Give the preparation type.
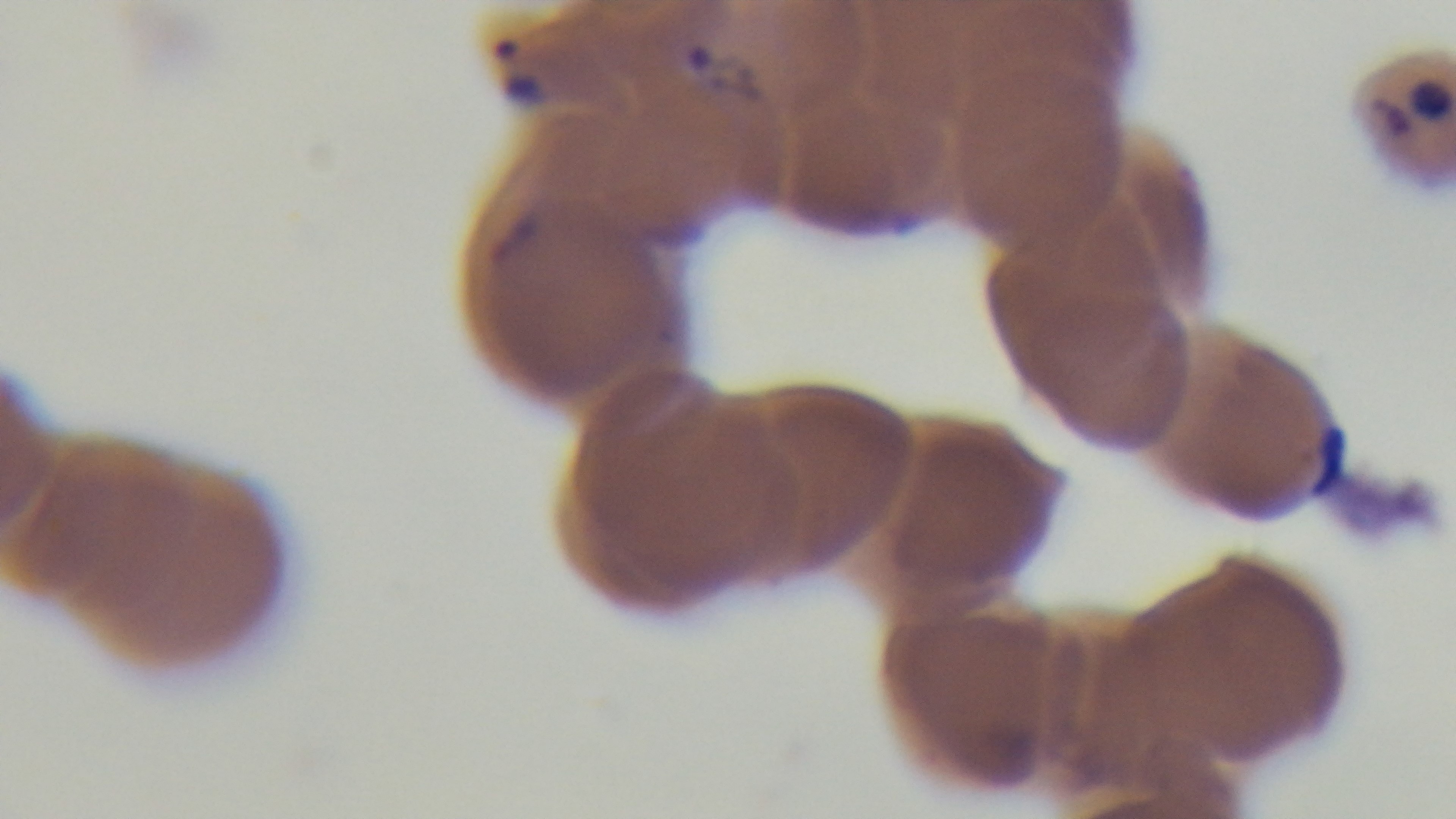
A thin smear.

Malaria status: positive. 100x oil-immersion objective. Single field of view. Giemsa-stained. Mounted 4K digital camera. Light microscopy.